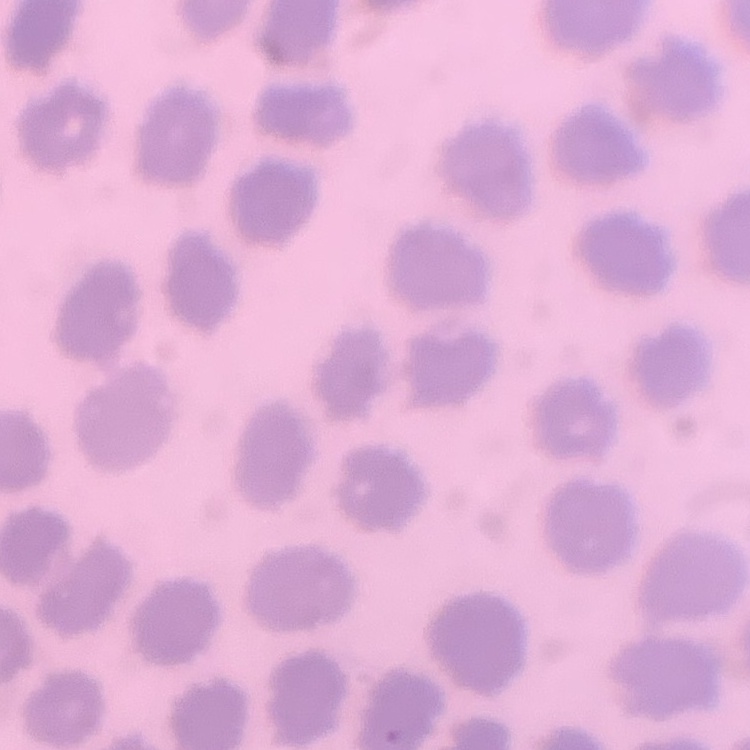
The red blood cells exhibit no rouleaux formation. Stained with either Field's or Giemsa. Square crop of a larger photomicrograph. Thin blood film.